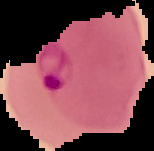

Image is 154×151 pixels. Cell region segmented out of the field of view; the surrounding area is masked to black. From a thin blood film. Malaria status: parasitized.